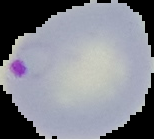
image type = segmented cell region with the area outside set to black
image size = 154×139 pixels
malaria status = parasitized
preparation = thin blood smear